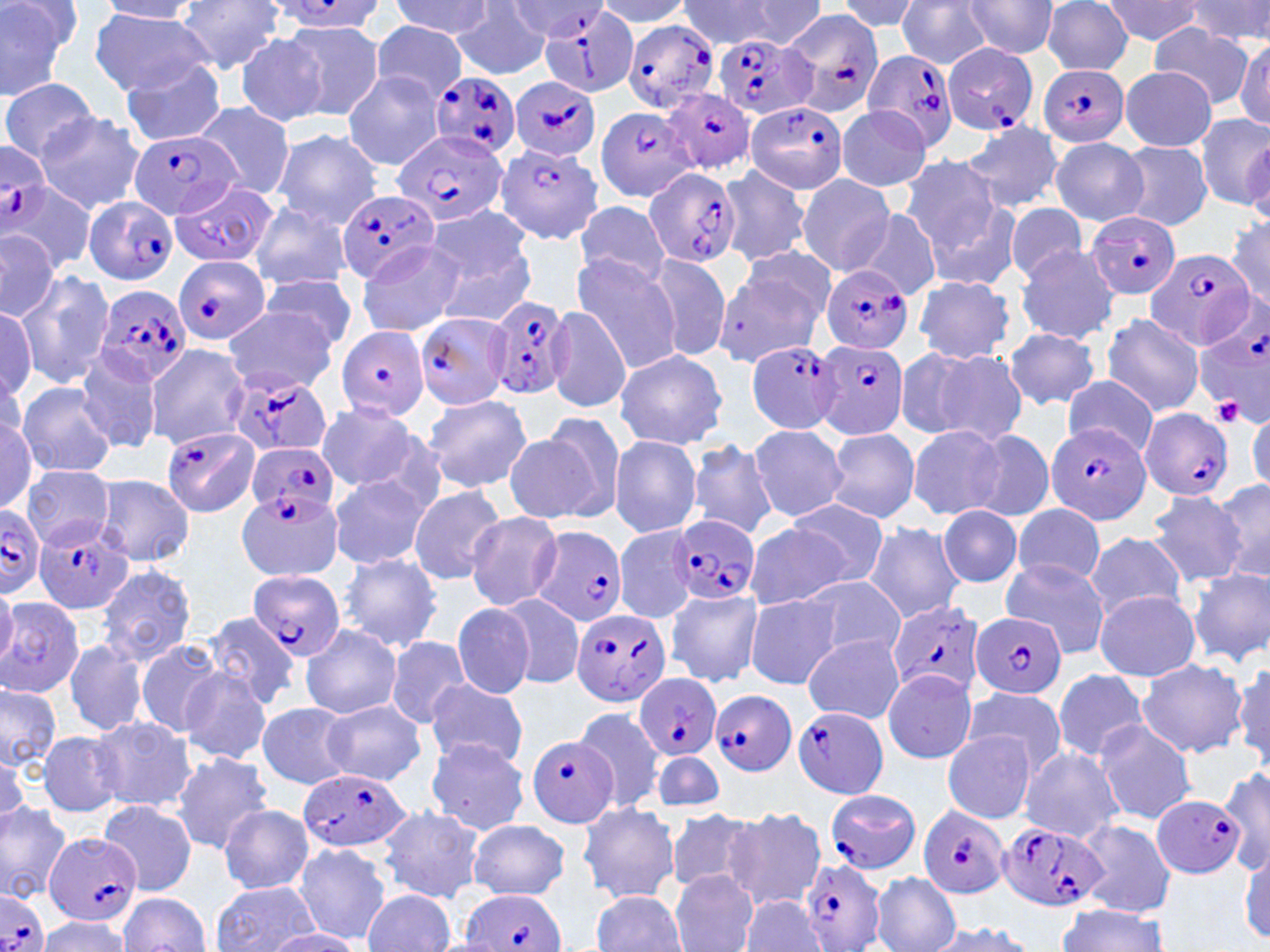
{
  "plasmodium_falciparum_infected_red_blood_cell_locations": "approximate bounding boxes as named x1/y1/x2/y2 corners in pixels: (x1=265, y1=2, x2=387, y2=34), (x1=542, y1=4, x2=639, y2=98), (x1=784, y1=10, x2=885, y2=116), (x1=622, y1=18, x2=720, y2=113), (x1=717, y1=34, x2=819, y2=120), (x1=942, y1=43, x2=1039, y2=136), (x1=861, y1=50, x2=958, y2=152), (x1=1037, y1=63, x2=1128, y2=148), (x1=430, y1=70, x2=519, y2=163), (x1=509, y1=77, x2=603, y2=163), (x1=664, y1=89, x2=754, y2=176), (x1=744, y1=102, x2=848, y2=195), (x1=593, y1=105, x2=696, y2=199), (x1=127, y1=128, x2=242, y2=219), (x1=394, y1=129, x2=507, y2=227), (x1=496, y1=141, x2=603, y2=247), (x1=1, y1=146, x2=49, y2=234), (x1=642, y1=166, x2=742, y2=269), (x1=165, y1=184, x2=278, y2=267), (x1=338, y1=191, x2=439, y2=286), (x1=83, y1=197, x2=178, y2=287), (x1=1086, y1=210, x2=1180, y2=301), (x1=1144, y1=246, x2=1254, y2=350), (x1=173, y1=255, x2=270, y2=343), (x1=820, y1=266, x2=913, y2=356), (x1=93, y1=283, x2=192, y2=386), (x1=480, y1=297, x2=569, y2=403), (x1=414, y1=312, x2=513, y2=409), (x1=1196, y1=314, x2=1269, y2=423), (x1=335, y1=326, x2=429, y2=421), (x1=815, y1=340, x2=909, y2=440), (x1=746, y1=341, x2=845, y2=435), (x1=225, y1=371, x2=332, y2=459), (x1=1138, y1=406, x2=1234, y2=500), (x1=1045, y1=422, x2=1152, y2=525), (x1=162, y1=425, x2=260, y2=516), (x1=245, y1=444, x2=339, y2=517), (x1=237, y1=489, x2=345, y2=582), (x1=0, y1=505, x2=46, y2=596), (x1=33, y1=513, x2=138, y2=615), (x1=669, y1=515, x2=760, y2=605), (x1=532, y1=527, x2=630, y2=626), (x1=248, y1=570, x2=343, y2=663), (x1=885, y1=600, x2=985, y2=697), (x1=569, y1=607, x2=672, y2=708), (x1=973, y1=610, x2=1067, y2=702), (x1=635, y1=673, x2=722, y2=761), (x1=709, y1=691, x2=797, y2=777), (x1=792, y1=707, x2=891, y2=798), (x1=524, y1=733, x2=619, y2=829), (x1=297, y1=770, x2=411, y2=854), (x1=823, y1=789, x2=922, y2=874), (x1=1152, y1=794, x2=1247, y2=879), (x1=917, y1=805, x2=1011, y2=898), (x1=997, y1=819, x2=1107, y2=913), (x1=44, y1=832, x2=141, y2=926), (x1=801, y1=857, x2=886, y2=952), (x1=460, y1=889, x2=567, y2=952), (x1=0, y1=891, x2=49, y2=952)",
  "slide_level_diagnosis": "Plasmodium falciparum",
  "field_of_view": "single",
  "uninfected_red_blood_cell_locations": "approximate bounding boxes as named x1/y1/x2/y2 corners in pixels: (x1=0, y1=0, x2=82, y2=101), (x1=593, y1=0, x2=695, y2=28), (x1=679, y1=0, x2=783, y2=49), (x1=833, y1=0, x2=923, y2=33), (x1=897, y1=0, x2=991, y2=69), (x1=1189, y1=0, x2=1270, y2=47), (x1=99, y1=1, x2=204, y2=22), (x1=174, y1=1, x2=288, y2=73), (x1=390, y1=1, x2=494, y2=39), (x1=717, y1=1, x2=829, y2=47), (x1=962, y1=1, x2=1058, y2=58), (x1=1040, y1=1, x2=1134, y2=74), (x1=1099, y1=1, x2=1205, y2=47), (x1=452, y1=5, x2=552, y2=79), (x1=89, y1=8, x2=215, y2=97), (x1=273, y1=20, x2=383, y2=121), (x1=369, y1=23, x2=468, y2=102), (x1=1152, y1=24, x2=1254, y2=106), (x1=234, y1=33, x2=327, y2=126), (x1=1236, y1=36, x2=1269, y2=127), (x1=119, y1=59, x2=225, y2=145), (x1=1119, y1=66, x2=1217, y2=151), (x1=343, y1=70, x2=446, y2=170), (x1=2, y1=78, x2=98, y2=162), (x1=192, y1=100, x2=296, y2=199), (x1=835, y1=106, x2=933, y2=193), (x1=35, y1=111, x2=145, y2=215), (x1=1195, y1=113, x2=1270, y2=211), (x1=960, y1=120, x2=1065, y2=215), (x1=271, y1=129, x2=384, y2=229), (x1=1050, y1=137, x2=1147, y2=226), (x1=1242, y1=137, x2=1269, y2=225), (x1=1115, y1=142, x2=1212, y2=230), (x1=898, y1=154, x2=1008, y2=259), (x1=717, y1=165, x2=811, y2=268), (x1=796, y1=174, x2=896, y2=277), (x1=2, y1=185, x2=96, y2=273), (x1=248, y1=199, x2=354, y2=290), (x1=573, y1=199, x2=671, y2=287), (x1=922, y1=199, x2=1022, y2=289), (x1=1006, y1=203, x2=1087, y2=282), (x1=424, y1=204, x2=534, y2=295), (x1=856, y1=210, x2=941, y2=300), (x1=1228, y1=213, x2=1270, y2=306), (x1=0, y1=231, x2=61, y2=323), (x1=355, y1=242, x2=467, y2=337), (x1=432, y1=242, x2=537, y2=328), (x1=1017, y1=244, x2=1119, y2=343), (x1=571, y1=253, x2=681, y2=372), (x1=644, y1=253, x2=732, y2=363), (x1=714, y1=255, x2=828, y2=366), (x1=15, y1=270, x2=116, y2=389), (x1=261, y1=273, x2=358, y2=354), (x1=911, y1=276, x2=1017, y2=362), (x1=0, y1=305, x2=36, y2=406), (x1=544, y1=305, x2=632, y2=413), (x1=220, y1=307, x2=341, y2=394), (x1=1101, y1=313, x2=1204, y2=418), (x1=1004, y1=327, x2=1100, y2=409), (x1=907, y1=344, x2=1028, y2=445), (x1=145, y1=346, x2=249, y2=451), (x1=613, y1=349, x2=729, y2=451), (x1=73, y1=350, x2=163, y2=454), (x1=1062, y1=377, x2=1158, y2=456), (x1=18, y1=383, x2=117, y2=478), (x1=422, y1=395, x2=532, y2=493), (x1=314, y1=403, x2=424, y2=493), (x1=0, y1=410, x2=41, y2=510), (x1=1247, y1=411, x2=1269, y2=496), (x1=527, y1=412, x2=627, y2=524), (x1=748, y1=423, x2=850, y2=523), (x1=906, y1=424, x2=1009, y2=522), (x1=824, y1=429, x2=920, y2=523), (x1=970, y1=430, x2=1054, y2=522), (x1=609, y1=435, x2=703, y2=538), (x1=686, y1=439, x2=779, y2=541), (x1=22, y1=464, x2=114, y2=548), (x1=93, y1=474, x2=194, y2=566), (x1=329, y1=474, x2=430, y2=569), (x1=1210, y1=478, x2=1270, y2=588), (x1=409, y1=484, x2=506, y2=585), (x1=1146, y1=492, x2=1246, y2=587), (x1=782, y1=500, x2=889, y2=588), (x1=1010, y1=503, x2=1108, y2=590), (x1=938, y1=505, x2=1024, y2=588), (x1=466, y1=511, x2=562, y2=612), (x1=863, y1=521, x2=964, y2=622), (x1=745, y1=522, x2=850, y2=612), (x1=614, y1=525, x2=696, y2=622), (x1=1085, y1=532, x2=1188, y2=621), (x1=340, y1=552, x2=442, y2=652), (x1=999, y1=558, x2=1111, y2=659), (x1=96, y1=563, x2=197, y2=667), (x1=1188, y1=565, x2=1270, y2=667), (x1=799, y1=576, x2=906, y2=661), (x1=0, y1=579, x2=17, y2=670), (x1=666, y1=588, x2=762, y2=687), (x1=1094, y1=590, x2=1200, y2=681), (x1=498, y1=592, x2=586, y2=692), (x1=0, y1=595, x2=94, y2=700), (x1=743, y1=595, x2=843, y2=688), (x1=452, y1=602, x2=536, y2=699), (x1=199, y1=613, x2=301, y2=710), (x1=300, y1=625, x2=401, y2=719), (x1=803, y1=634, x2=904, y2=723), (x1=384, y1=636, x2=472, y2=728), (x1=63, y1=639, x2=150, y2=739), (x1=134, y1=639, x2=225, y2=739), (x1=1135, y1=658, x2=1248, y2=758), (x1=1232, y1=659, x2=1269, y2=770), (x1=179, y1=666, x2=274, y2=767), (x1=1051, y1=668, x2=1149, y2=762), (x1=882, y1=669, x2=977, y2=764), (x1=425, y1=679, x2=529, y2=769), (x1=0, y1=682, x2=63, y2=772), (x1=957, y1=689, x2=1067, y2=778), (x1=322, y1=700, x2=425, y2=785), (x1=257, y1=703, x2=354, y2=788), (x1=573, y1=706, x2=666, y2=811), (x1=90, y1=717, x2=196, y2=812), (x1=1093, y1=720, x2=1198, y2=823), (x1=36, y1=730, x2=127, y2=818), (x1=942, y1=730, x2=1036, y2=825), (x1=423, y1=736, x2=530, y2=835), (x1=0, y1=747, x2=29, y2=833), (x1=1018, y1=747, x2=1124, y2=843), (x1=650, y1=752, x2=726, y2=810), (x1=170, y1=753, x2=275, y2=853), (x1=1219, y1=766, x2=1270, y2=875), (x1=0, y1=799, x2=73, y2=902), (x1=99, y1=799, x2=198, y2=895), (x1=577, y1=801, x2=679, y2=902), (x1=217, y1=804, x2=314, y2=893), (x1=378, y1=806, x2=485, y2=902), (x1=723, y1=807, x2=827, y2=910), (x1=665, y1=810, x2=759, y2=894), (x1=1075, y1=819, x2=1177, y2=916), (x1=464, y1=821, x2=572, y2=899), (x1=293, y1=844, x2=390, y2=944), (x1=1240, y1=854, x2=1270, y2=943), (x1=669, y1=871, x2=758, y2=952), (x1=871, y1=872, x2=959, y2=952), (x1=211, y1=881, x2=322, y2=952), (x1=364, y1=889, x2=455, y2=951), (x1=590, y1=890, x2=687, y2=951), (x1=117, y1=893, x2=212, y2=950), (x1=739, y1=899, x2=827, y2=951), (x1=1056, y1=905, x2=1171, y2=951), (x1=33, y1=917, x2=134, y2=951), (x1=919, y1=920, x2=1038, y2=952), (x1=264, y1=929, x2=362, y2=951)",
  "platelet_locations": "approximate bounding boxes as named x1/y1/x2/y2 corners in pixels: (x1=1213, y1=396, x2=1243, y2=427)",
  "magnification": "1000x",
  "stain": "May-Grünwald-Giemsa",
  "modality": "optical microscopy",
  "preparation": "thin blood smear",
  "image_size": "1270×952 pixels"
}